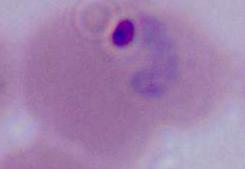
Summary:
  - Magnification: 400x or 1000x
  - Identification: Plasmodium
  - Modality: micrograph